Identify the preparation type.
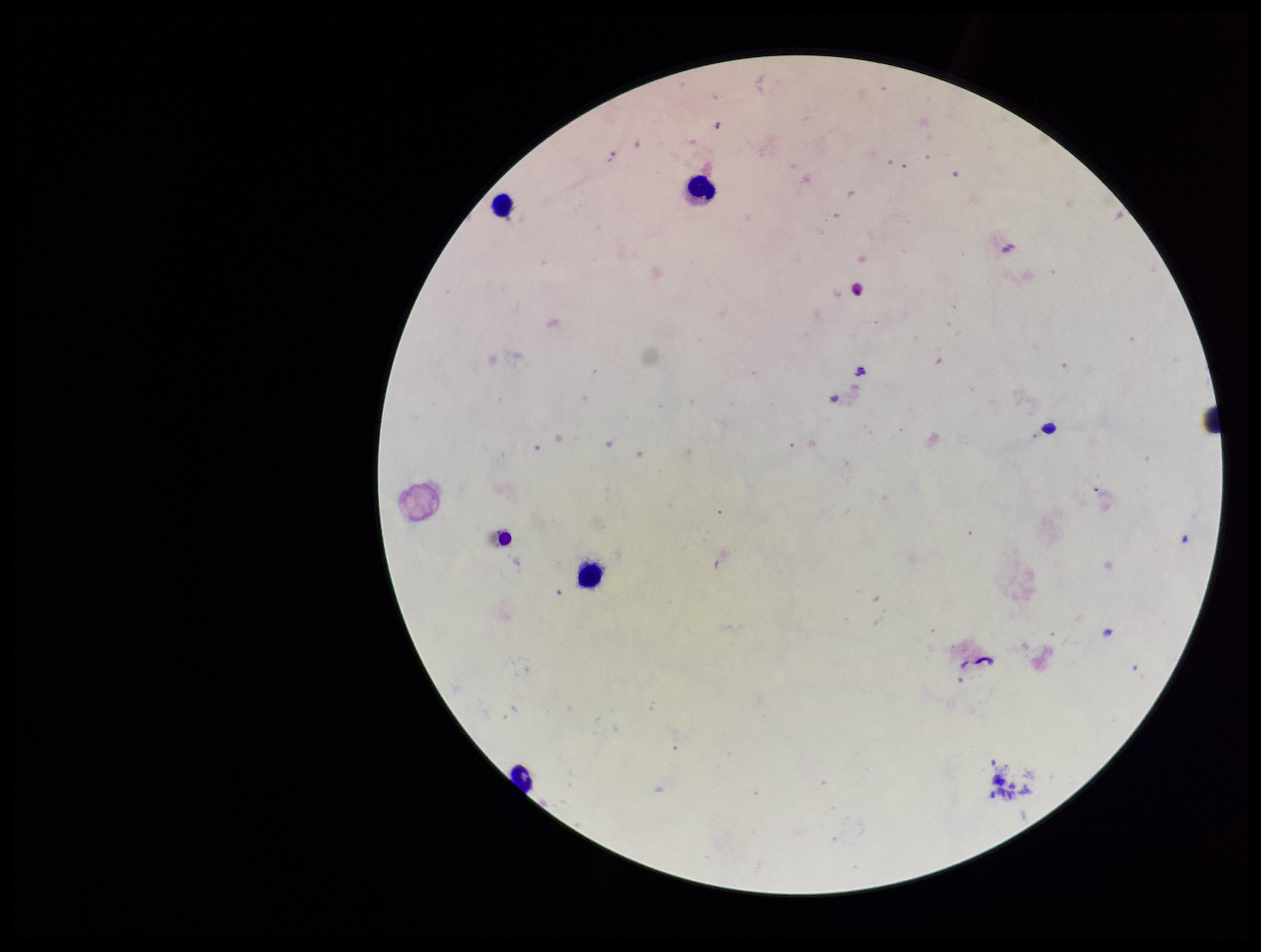

It is a thick blood smear.

Patient malaria status: negative. Leukocyte count: 5. Parasite count: 0. Smartphone photograph taken through the eyepiece of a microscope. Giemsa stain. Plasmodium parasites: none identified. Single field of view. Image is 1261×952 pixels.